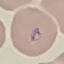

Result: malaria parasites detected. Thin smear of blood. Acquired by smartphone through the microscope eyepiece. Cell patch, automatically extracted from a larger field of view and resized to 64 × 64 pixels. Giemsa-stained preparation.